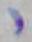

{
  "modality": "micrograph",
  "magnification": "1000x",
  "identification": "Toxoplasma gondii"
}